Classify this cell by malaria status.
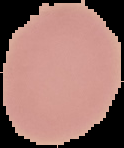
It is uninfected.

Summary:
  - Image size: 124×148 pixels
  - Image type: segmented cell region on a black background
  - Preparation: thin blood smear